Look for Plasmodium parasites.
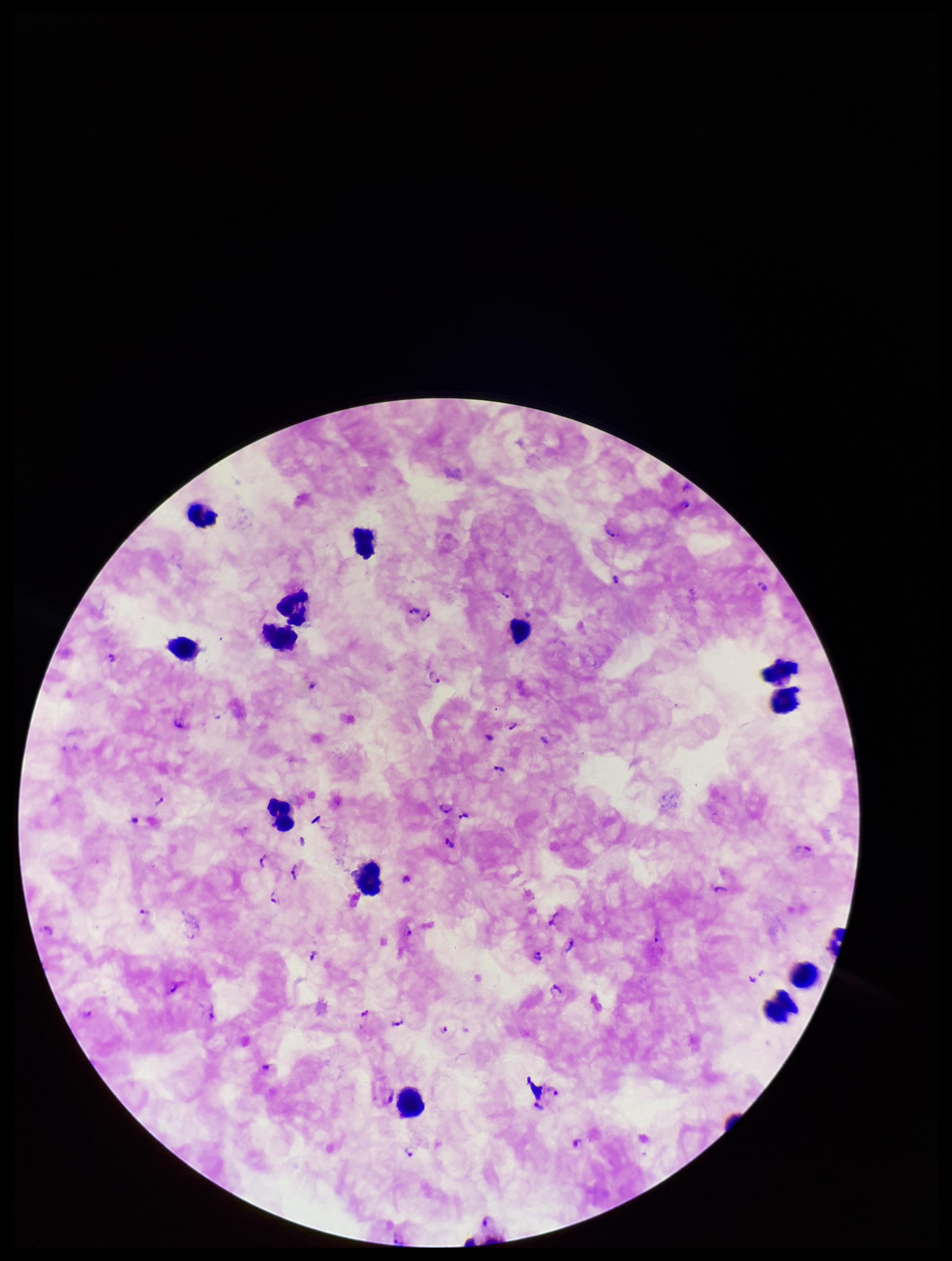

Seen.

Summary:
  - Parasite count: 38
  - Patient malaria status: positive
  - Species reported for this patient: Plasmodium falciparum
  - Stain: Giemsa
  - Preparation: thick blood smear
  - Capture: smartphone photograph through the microscope eyepiece
  - Field of view: single
  - Image size: 952×1261 pixels
  - Leukocyte count: 14